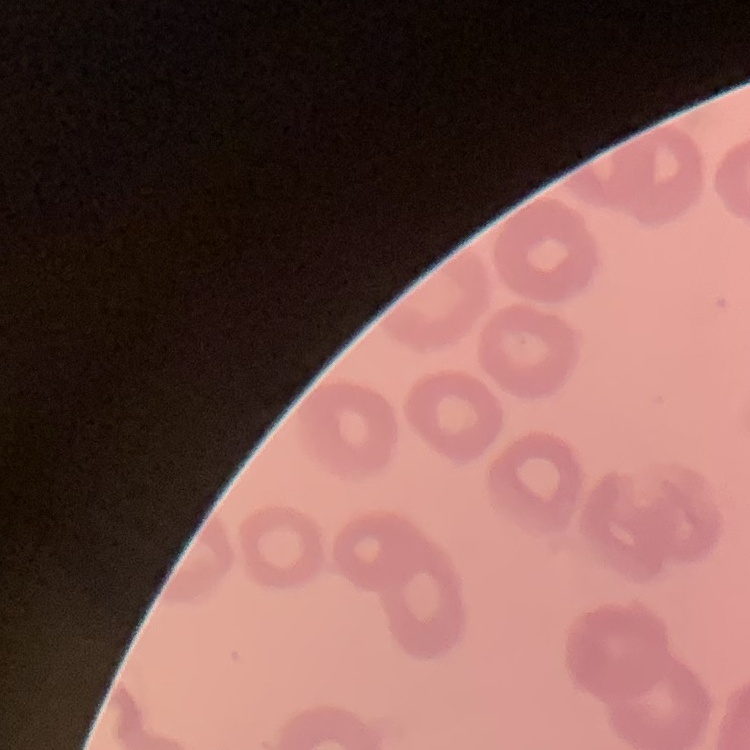
Summary:
  - Erythrocyte morphology: no rouleaux formation
  - Image type: one tile cut from a larger photomicrograph
  - Stain: Field's or Giemsa
  - Preparation: thin blood film